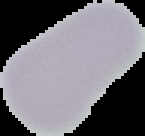
Summary:
  - Image type: segmented cell region with the area outside set to black
  - Image size: 145×136 pixels
  - Preparation: thin blood smear
  - Malaria status: uninfected